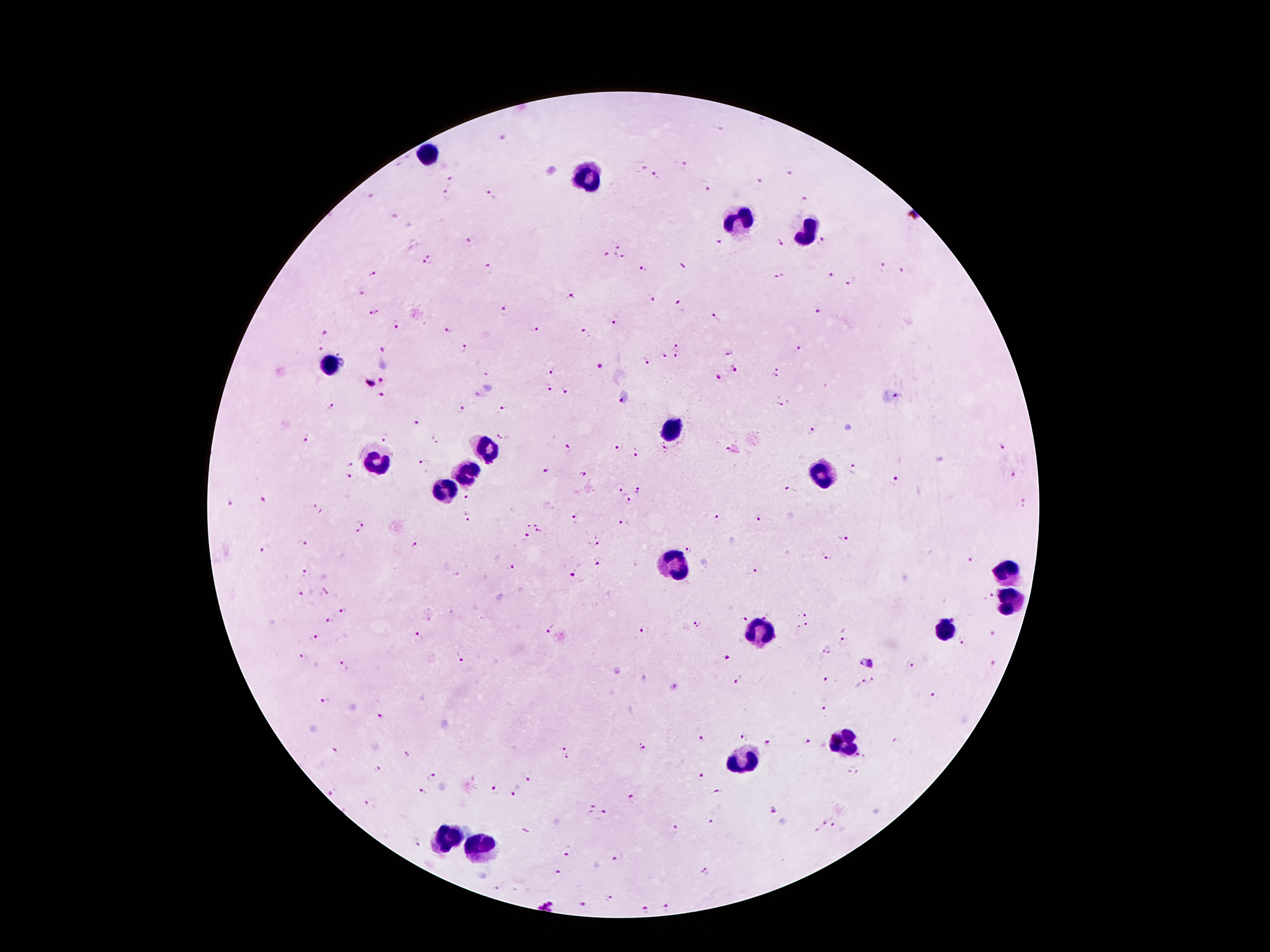
image_size: 1270×952 pixels
field_of_view: single
capture: smartphone through the microscope eyepiece
malaria_parasite_locations: 'approximate centers as [x, y] in pixels: [684, 165], [643, 167], [789, 173], [656, 175], [451, 181], [760, 181], [706, 190], [447, 195], [368, 196], [491, 196], [805, 199], [471, 241], [719, 242], [825, 242], [780, 244], [617, 247], [608, 254], [622, 257], [428, 260], [489, 269], [643, 269], [883, 269], [904, 271], [371, 275], [833, 275], [780, 276], [849, 280], [363, 291], [652, 298], [570, 299], [679, 304], [818, 309], [505, 311], [373, 312], [716, 319], [616, 322], [397, 324], [533, 328], [449, 330], [586, 333], [326, 335], [679, 347], [464, 348], [320, 349], [385, 349], [798, 350], [728, 351], [339, 353], [663, 356], [674, 359], [647, 362], [598, 365], [551, 369], [735, 369], [777, 372], [717, 377], [383, 380], [369, 384], [548, 387], [566, 392], [382, 394], [899, 397], [622, 399], [779, 405], [332, 407], [462, 410], [502, 410], [417, 421], [812, 431], [384, 436], [307, 437], [502, 437], [436, 438], [618, 446], [1003, 447], [568, 448], [667, 449], [636, 453], [425, 463], [348, 464], [854, 469], [546, 471], [584, 473], [350, 475], [1014, 476], [894, 482], [790, 490], [638, 491], [621, 493], [466, 499], [261, 500], [628, 501], [229, 503], [1024, 503], [318, 508], [717, 515], [467, 516], [757, 518], [577, 519], [623, 522], [532, 524], [360, 527], [539, 531], [527, 536], [843, 539], [598, 540], [302, 542], [415, 544], [264, 548], [687, 549], [830, 557], [970, 561], [598, 563], [510, 566], [751, 572], [304, 573], [574, 573], [301, 593], [990, 597], [342, 611], [766, 615], [801, 615], [742, 619], [330, 621], [697, 624], [804, 625], [551, 628], [644, 630], [992, 634], [313, 635], [421, 636], [963, 641], [842, 642], [826, 651], [303, 656], [461, 658], [726, 658], [343, 662], [861, 662], [872, 663], [994, 663], [911, 665], [828, 679], [737, 681], [871, 681], [859, 683], [932, 695], [325, 701], [825, 706], [381, 716], [741, 737], [702, 738], [896, 740], [769, 742], [807, 742], [645, 746], [561, 748], [336, 752], [407, 754], [860, 755], [568, 758], [377, 770], [853, 770], [701, 775], [432, 778], [527, 778], [495, 790], [423, 792], [333, 793], [717, 793], [513, 794], [633, 799], [369, 805], [589, 807], [773, 811], [602, 815], [711, 820], [826, 822], [835, 826], [674, 828], [815, 830], [418, 842], [568, 854], [617, 857], [705, 870], [557, 872], [496, 889], [609, 899], [582, 903], [546, 904], [665, 907], [643, 910]'
patient_malaria_status: infected with Plasmodium falciparum
leukocyte_locations: 'approximate centers as [x, y] in pixels: [431, 156], [583, 176], [742, 221], [808, 230], [331, 364], [673, 433], [487, 449], [377, 461], [470, 470], [825, 472], [446, 490], [673, 567], [1006, 570], [1011, 601], [757, 628], [944, 631], [843, 746], [744, 761], [444, 836], [484, 845]'
preparation: thick blood smear
magnification: 100x
stain: Giemsa